Assess the morphology of the red blood cells.
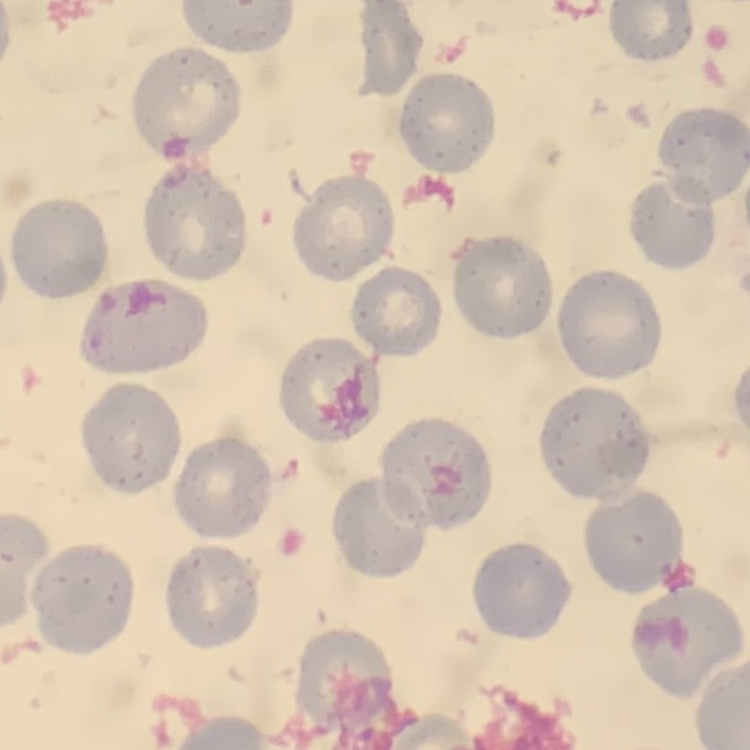

No rouleaux formation.

stain: Field's or Giemsa
image_type: one tile cut from a larger photomicrograph
preparation: thin blood film